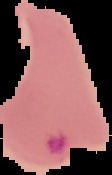
image_type: segmented cell region on a black background
malaria_status: parasitized
image_size: 112×175 pixels
preparation: thin blood smear